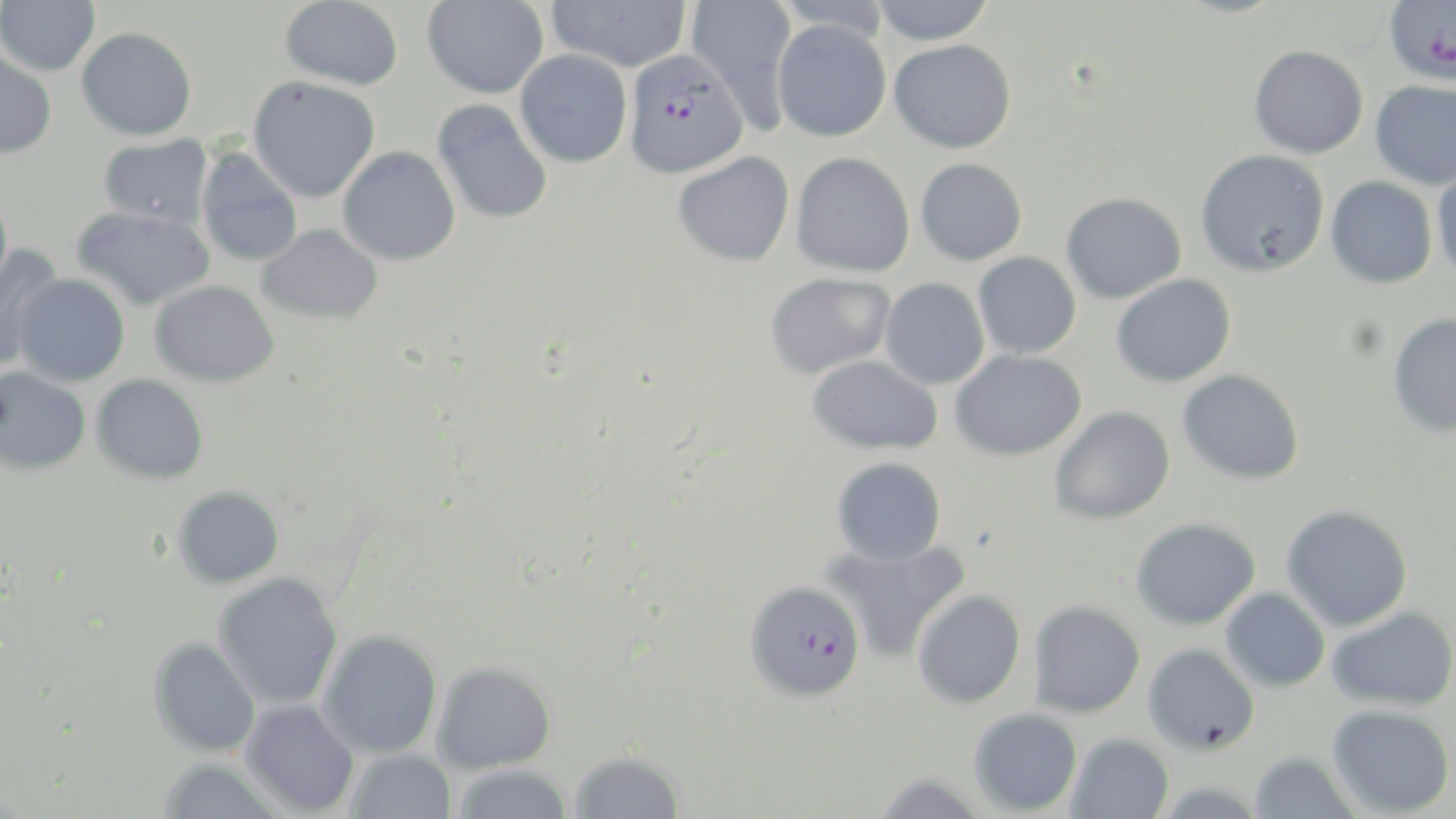
slide_level_diagnosis: Plasmodium falciparum
image_size: 1456×819 pixels
field_of_view: single
stain: May-Grünwald-Giemsa
modality: light microscopy
plasmodium_falciparum_infected_red_blood_cell_locations: 'approximate bounding boxes as named x1/y1/x2/y2 corners in pixels: (x1=1383, y1=0, x2=1456, y2=86), (x1=623, y1=48, x2=749, y2=179), (x1=745, y1=579, x2=866, y2=701)'
preparation: thin blood smear
uninfected_red_blood_cell_locations: 'approximate bounding boxes as named x1/y1/x2/y2 corners in pixels: (x1=0, y1=0, x2=100, y2=76), (x1=280, y1=0, x2=403, y2=89), (x1=547, y1=0, x2=691, y2=72), (x1=684, y1=0, x2=800, y2=131), (x1=772, y1=0, x2=894, y2=40), (x1=870, y1=0, x2=996, y2=45), (x1=422, y1=1, x2=548, y2=99), (x1=772, y1=19, x2=891, y2=142), (x1=76, y1=27, x2=196, y2=141), (x1=889, y1=39, x2=1017, y2=153), (x1=1249, y1=44, x2=1369, y2=158), (x1=0, y1=49, x2=57, y2=158), (x1=515, y1=50, x2=632, y2=168), (x1=248, y1=76, x2=380, y2=203), (x1=1369, y1=79, x2=1456, y2=190), (x1=432, y1=98, x2=553, y2=225), (x1=98, y1=135, x2=213, y2=229), (x1=338, y1=146, x2=461, y2=265), (x1=196, y1=147, x2=303, y2=267), (x1=1195, y1=148, x2=1330, y2=277), (x1=672, y1=151, x2=795, y2=266), (x1=791, y1=152, x2=915, y2=277), (x1=915, y1=157, x2=1026, y2=266), (x1=1431, y1=165, x2=1456, y2=284), (x1=1325, y1=176, x2=1437, y2=288), (x1=1061, y1=192, x2=1186, y2=304), (x1=72, y1=205, x2=214, y2=311), (x1=256, y1=223, x2=383, y2=324), (x1=0, y1=244, x2=65, y2=375), (x1=973, y1=252, x2=1081, y2=358), (x1=765, y1=272, x2=896, y2=378), (x1=13, y1=274, x2=130, y2=386), (x1=1111, y1=274, x2=1236, y2=387), (x1=880, y1=277, x2=990, y2=389), (x1=150, y1=280, x2=279, y2=387), (x1=1387, y1=311, x2=1456, y2=438), (x1=950, y1=349, x2=1087, y2=460), (x1=807, y1=355, x2=943, y2=455), (x1=0, y1=366, x2=91, y2=475), (x1=1177, y1=369, x2=1305, y2=485), (x1=92, y1=374, x2=209, y2=484), (x1=1049, y1=406, x2=1175, y2=524), (x1=831, y1=456, x2=947, y2=565), (x1=172, y1=486, x2=284, y2=588), (x1=1281, y1=505, x2=1413, y2=631), (x1=1131, y1=518, x2=1260, y2=630), (x1=822, y1=539, x2=971, y2=662), (x1=212, y1=572, x2=344, y2=710), (x1=1220, y1=588, x2=1330, y2=692), (x1=912, y1=589, x2=1027, y2=708), (x1=1028, y1=600, x2=1146, y2=717), (x1=1327, y1=606, x2=1455, y2=711), (x1=317, y1=630, x2=442, y2=758), (x1=148, y1=637, x2=262, y2=757), (x1=1142, y1=642, x2=1261, y2=754), (x1=431, y1=662, x2=556, y2=774), (x1=240, y1=699, x2=359, y2=816), (x1=1327, y1=704, x2=1454, y2=817), (x1=969, y1=708, x2=1082, y2=816), (x1=1065, y1=733, x2=1174, y2=819), (x1=344, y1=749, x2=457, y2=819), (x1=568, y1=751, x2=685, y2=818), (x1=1248, y1=752, x2=1361, y2=819), (x1=157, y1=758, x2=285, y2=819), (x1=450, y1=764, x2=574, y2=819), (x1=869, y1=773, x2=989, y2=818)'
magnification: 1000x